Assess this cell for malaria.
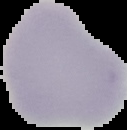

Uninfected.

image type = segmented cell region on a black background
preparation = thin blood film
image size = 127×130 pixels